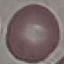

Result: no malaria parasites detected. Cell patch, automatically extracted from a larger field of view and resized to 64 × 64 pixels. Thin blood smear. Giemsa stain. Acquired by smartphone through the microscope eyepiece.